Outline each blood parasite and name the species.
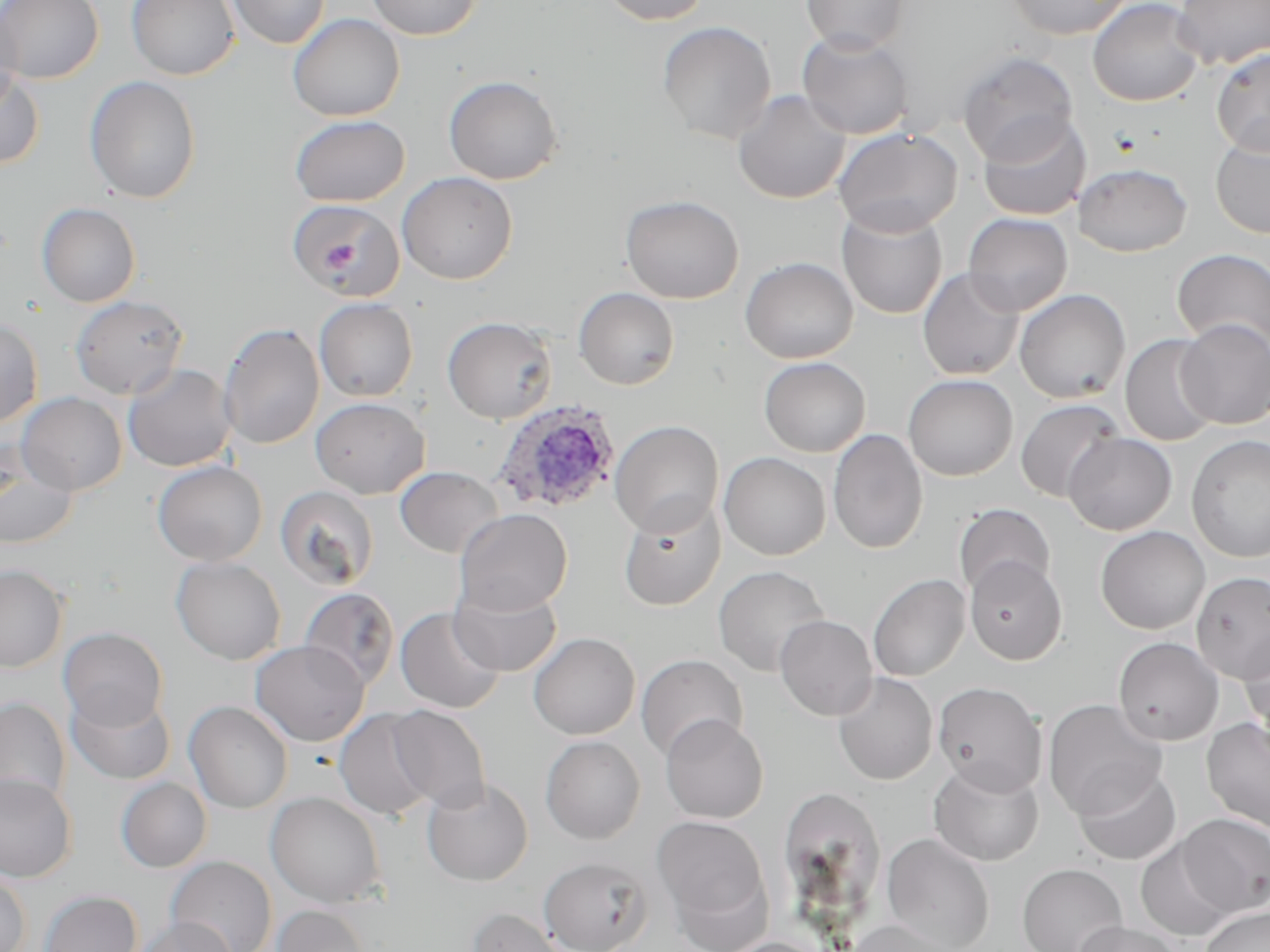
Approximate bounding boxes as [x1, y1, x2, y2] in pixels.
Plasmodium ovale-infected red blood cells: [492, 400, 620, 515].
No Plasmodium falciparum, Plasmodium malariae, Plasmodium vivax, Babesia divergens, or Trypanosoma brucei observed.

Uninfected red blood cell locations: [0, 0, 104, 84], [126, 0, 240, 80], [227, 0, 331, 49], [365, 0, 482, 40], [601, 0, 711, 25], [801, 0, 908, 54], [1005, 0, 1133, 39], [1087, 0, 1205, 107], [1173, 0, 1270, 69], [0, 3, 23, 113], [288, 13, 405, 122], [657, 21, 777, 144], [797, 30, 915, 140], [1210, 48, 1270, 156], [957, 51, 1078, 165], [0, 68, 46, 169], [443, 75, 563, 184], [84, 76, 202, 204], [732, 90, 851, 204], [977, 113, 1090, 221], [289, 115, 410, 207], [832, 127, 963, 236], [1210, 133, 1270, 239], [1075, 163, 1193, 257], [397, 171, 517, 285], [620, 194, 744, 303], [285, 198, 407, 300], [37, 203, 141, 307], [836, 204, 948, 320], [963, 213, 1073, 316], [1171, 249, 1270, 352], [740, 256, 859, 364], [917, 267, 1024, 380], [573, 287, 680, 390], [1014, 289, 1131, 403], [69, 295, 189, 400], [314, 298, 418, 402], [442, 316, 558, 424], [0, 317, 44, 426], [1176, 318, 1270, 430], [218, 322, 325, 449], [1119, 334, 1221, 448], [759, 356, 870, 457], [122, 363, 237, 472], [903, 374, 1018, 481], [17, 393, 127, 496], [310, 396, 430, 499], [1014, 399, 1125, 503], [610, 420, 724, 537], [828, 428, 928, 554], [1063, 432, 1177, 535], [1186, 435, 1270, 562], [0, 443, 79, 550], [718, 452, 831, 560], [151, 460, 267, 565], [394, 466, 505, 559], [275, 485, 380, 591], [618, 498, 726, 611], [953, 503, 1056, 600], [454, 508, 572, 616], [1095, 525, 1210, 634], [964, 555, 1067, 665], [170, 556, 286, 665], [0, 564, 68, 673], [713, 565, 830, 677], [1190, 570, 1270, 683], [867, 574, 970, 681], [449, 582, 562, 677], [299, 587, 400, 691], [395, 606, 506, 714], [774, 614, 878, 721], [1239, 626, 1270, 742], [58, 627, 168, 730], [528, 632, 640, 740], [1113, 637, 1224, 746], [250, 640, 369, 746], [636, 654, 748, 761], [832, 672, 938, 785], [933, 681, 1047, 795], [66, 688, 176, 785], [931, 689, 1164, 802], [0, 696, 70, 809], [1043, 699, 1167, 820], [183, 700, 294, 814], [385, 705, 491, 812], [334, 707, 438, 821], [660, 713, 768, 823], [1201, 718, 1270, 833], [540, 735, 645, 844], [928, 759, 1044, 866], [1072, 764, 1181, 866], [0, 772, 78, 882], [421, 776, 534, 886], [115, 777, 212, 873], [790, 791, 879, 918], [265, 792, 387, 908], [1177, 814, 1270, 917], [652, 815, 771, 935], [881, 833, 995, 952], [1134, 838, 1237, 942], [166, 855, 277, 952], [539, 857, 652, 952], [1017, 863, 1127, 952], [0, 871, 31, 951], [39, 890, 142, 952], [270, 904, 372, 952], [466, 906, 571, 952], [1201, 906, 1270, 952], [135, 917, 238, 952], [844, 920, 958, 952], [1073, 921, 1184, 952], [716, 937, 830, 952]. Slide-level diagnosis: Plasmodium ovale. Captured at 1000x magnification. May-Grünwald-Giemsa-stained preparation. Image is 1270×952 pixels. Thin blood smear. Light microscopy. One field of a larger specimen.